State the preparation type.
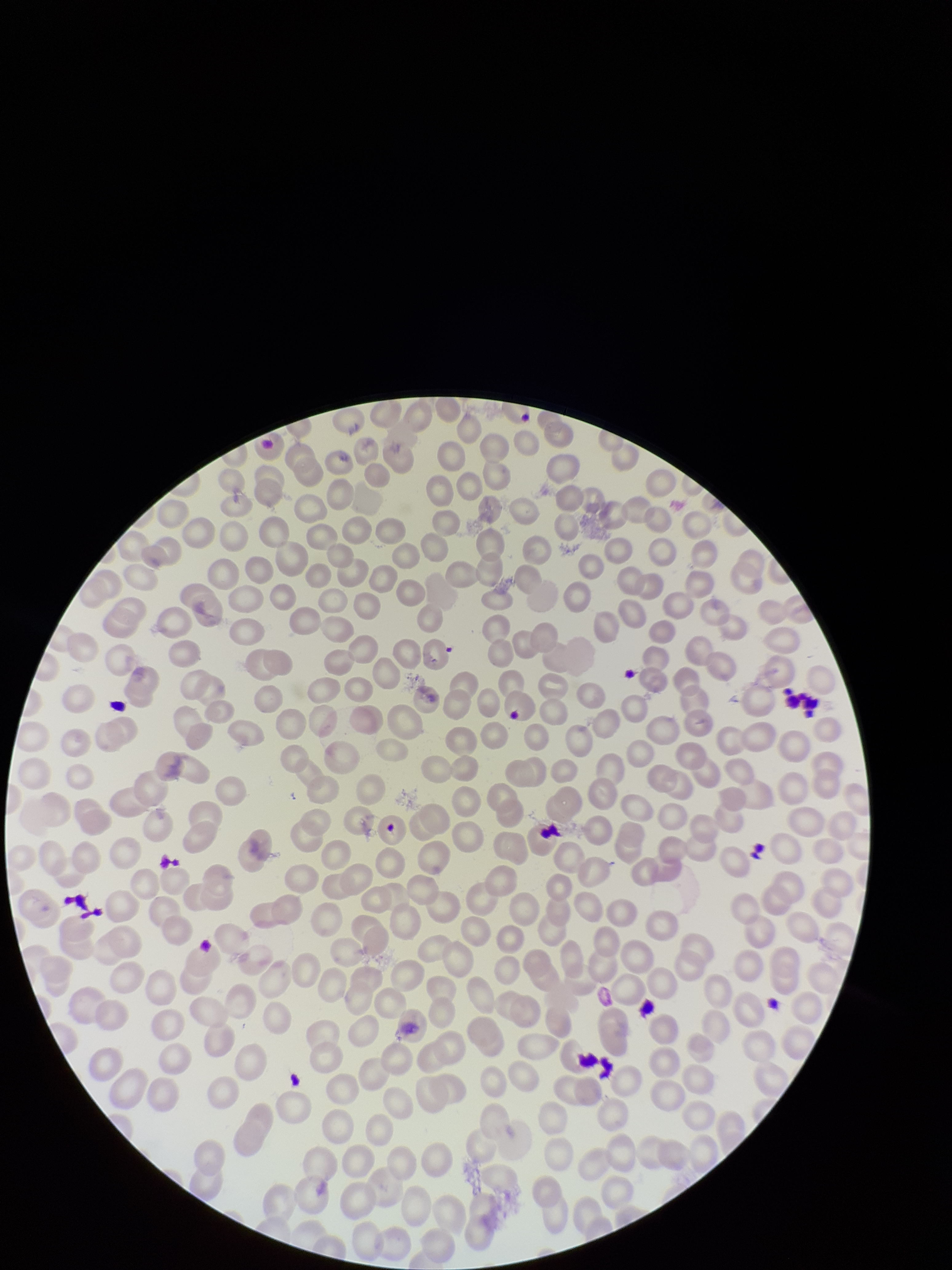

Thin.

patient malaria status = negative
image size = 952×1270 pixels
parasitized red blood cell count = 0
capture = smartphone photograph through the microscope eyepiece
red blood cell count = 264
stain = Giemsa
field of view = one from this slide
parasitized red blood cells = none detected